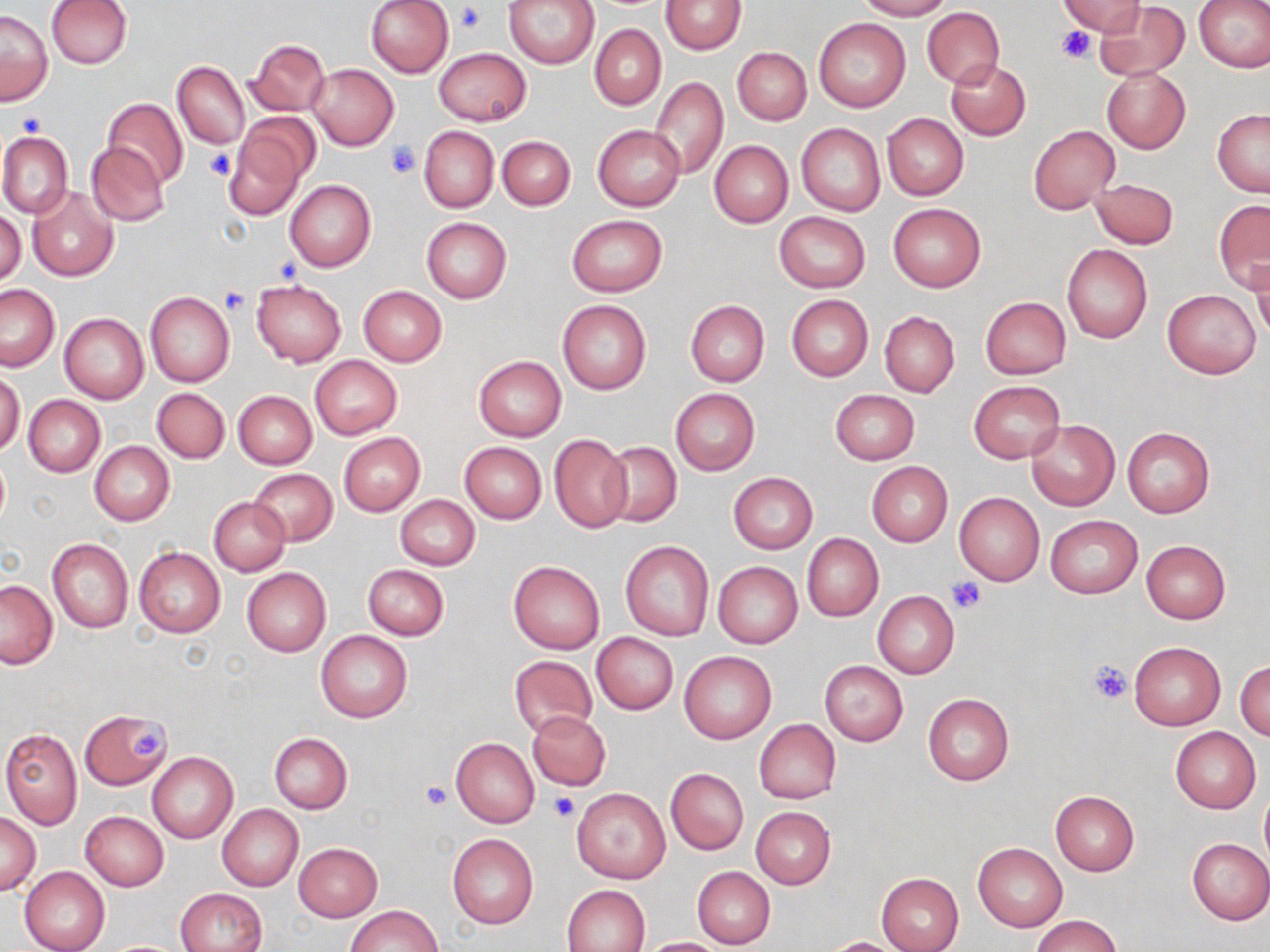

slide-level diagnosis = negative for blood parasites
stain = May-Grünwald-Giemsa
field of view = one of a larger specimen
modality = light microscopy
image size = 1270×952 pixels
magnification = 1000x
platelet locations = approximate bounding boxes as (x1, y1, x2, y2) in pixels: (458, 3, 487, 33), (1056, 25, 1097, 63), (14, 112, 44, 138), (386, 141, 418, 176), (204, 148, 237, 181), (219, 286, 251, 314), (946, 578, 985, 613), (1088, 657, 1134, 705), (128, 729, 168, 758), (422, 781, 451, 810), (550, 791, 579, 821)
uninfected red blood cell locations = approximate bounding boxes as (x1, y1, x2, y2) in pixels: (45, 0, 132, 69), (365, 0, 454, 77), (502, 0, 600, 68), (660, 0, 747, 54), (854, 0, 951, 21), (1056, 0, 1146, 37), (1194, 0, 1270, 73), (1094, 1, 1189, 82), (922, 7, 1004, 88), (1, 9, 52, 105), (813, 18, 911, 113), (590, 24, 666, 110), (246, 38, 330, 116), (732, 46, 811, 125), (434, 47, 531, 126), (945, 59, 1031, 141), (173, 61, 249, 148), (308, 64, 399, 150), (1102, 68, 1191, 153), (651, 78, 728, 178), (102, 98, 188, 187), (1212, 109, 1270, 197), (882, 114, 968, 200), (225, 115, 315, 217), (796, 123, 885, 217), (593, 124, 684, 212), (1028, 125, 1120, 214), (418, 126, 498, 213), (0, 131, 73, 218), (497, 136, 575, 211), (709, 140, 793, 228), (86, 143, 169, 226), (1089, 177, 1179, 249), (285, 179, 376, 271), (27, 188, 118, 281), (1214, 200, 1270, 292), (888, 203, 986, 292), (0, 209, 25, 287), (774, 211, 870, 293), (568, 214, 667, 295), (421, 217, 511, 302), (1061, 244, 1153, 343), (1249, 258, 1270, 339), (251, 279, 346, 366), (0, 283, 60, 372), (357, 285, 447, 367), (1162, 290, 1260, 379), (145, 292, 235, 386), (786, 295, 873, 381), (980, 297, 1071, 379), (557, 300, 651, 394), (684, 301, 769, 387), (879, 311, 959, 398), (59, 312, 149, 403), (309, 356, 402, 439), (473, 356, 566, 441), (1, 370, 25, 456), (970, 380, 1065, 465), (152, 388, 229, 463), (670, 388, 759, 475), (831, 389, 920, 465), (232, 391, 317, 470), (24, 395, 105, 476), (1026, 419, 1120, 510), (1122, 427, 1216, 517), (339, 432, 425, 515), (548, 434, 632, 532), (89, 440, 174, 526), (602, 441, 682, 527), (459, 442, 547, 522), (0, 454, 10, 532), (866, 462, 953, 547), (248, 469, 338, 545), (728, 472, 817, 552), (954, 493, 1045, 585), (395, 496, 481, 570), (208, 497, 290, 576), (1046, 515, 1143, 598), (802, 533, 883, 622), (47, 539, 133, 633), (1141, 540, 1231, 623), (620, 541, 714, 641), (134, 546, 225, 637), (508, 559, 605, 653), (713, 562, 803, 649), (362, 564, 450, 640), (242, 567, 331, 657), (1, 580, 58, 669), (873, 591, 959, 679), (316, 629, 412, 723), (592, 632, 679, 714), (1129, 642, 1225, 731), (680, 652, 776, 742), (510, 656, 597, 738), (1236, 659, 1270, 741), (819, 660, 908, 746), (923, 693, 1015, 786), (80, 710, 172, 790), (527, 711, 610, 790), (754, 719, 841, 803), (1170, 725, 1261, 813), (1, 728, 83, 828), (270, 733, 352, 813), (451, 737, 539, 828), (148, 751, 237, 844), (665, 768, 748, 855), (572, 787, 671, 884), (1259, 790, 1270, 868), (1051, 791, 1139, 876), (218, 805, 303, 890), (750, 807, 835, 889), (0, 812, 40, 895), (80, 812, 168, 891), (447, 834, 539, 929), (1186, 839, 1270, 924), (293, 843, 382, 921), (973, 843, 1067, 931), (20, 867, 110, 952), (692, 867, 775, 949), (876, 873, 964, 952), (562, 885, 649, 951), (175, 887, 268, 952), (346, 904, 442, 952), (1032, 915, 1121, 952), (638, 937, 730, 951), (821, 937, 910, 952)
preparation = thin blood smear